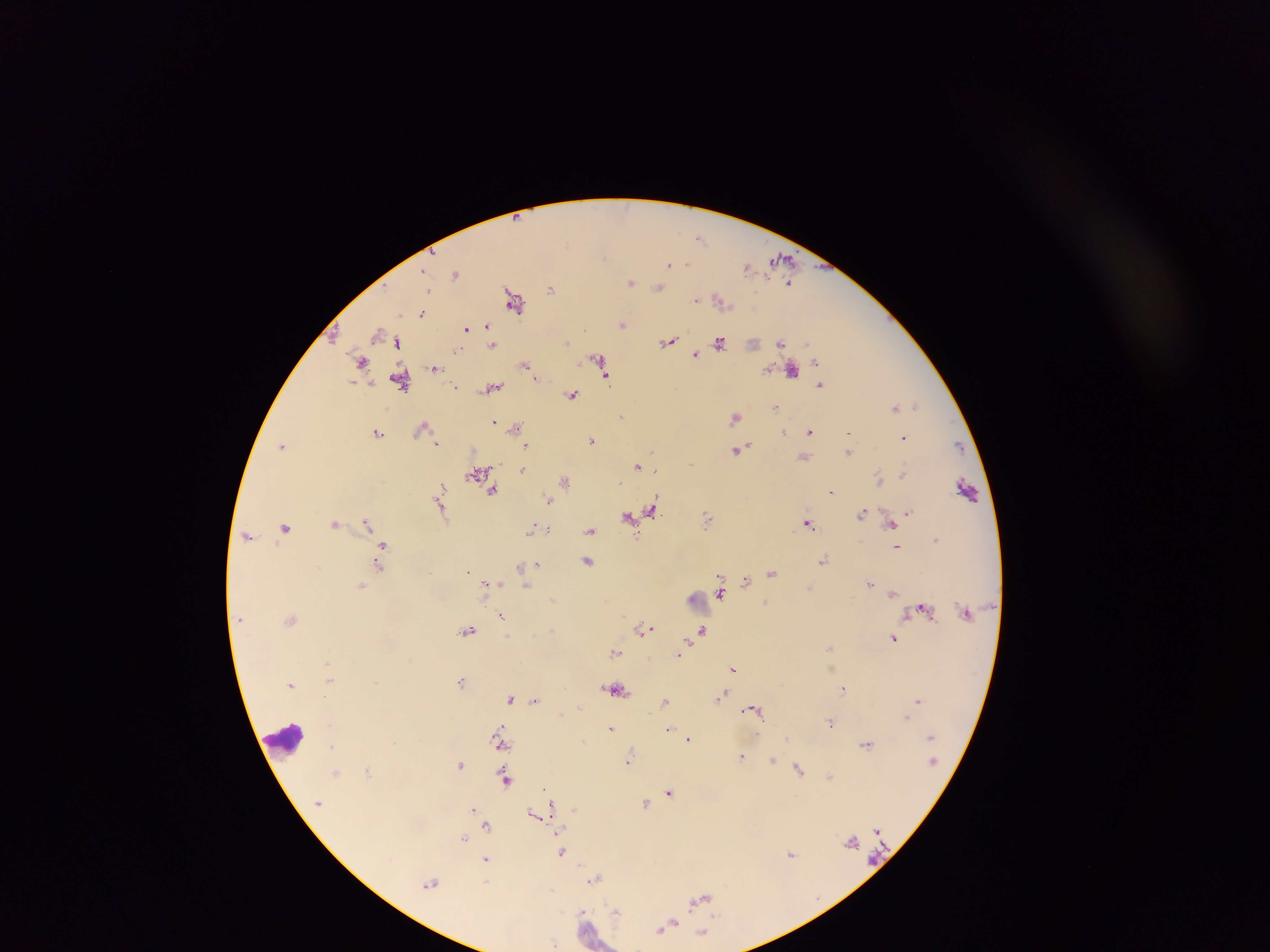

capture = mobile-phone photograph through a microscope
image size = 1270×952 pixels
field of view = single
malaria parasite locations = approximate centers as {x, y} in pixels: {700, 238}, {783, 260}, {670, 264}, {747, 266}, {425, 272}, {455, 273}, {631, 281}, {790, 283}, {659, 286}, {429, 288}, {551, 288}, {514, 299}, {696, 299}, {721, 300}, {422, 314}, {623, 323}, {488, 326}, {466, 327}, {399, 340}, {669, 341}, {719, 342}, {754, 342}, {782, 343}, {493, 344}, {695, 353}, {601, 359}, {816, 360}, {362, 361}, {526, 365}, {435, 367}, {768, 368}, {792, 369}, {607, 374}, {401, 380}, {354, 383}, {821, 383}, {455, 386}, {493, 387}, {572, 395}, {918, 405}, {895, 407}, {774, 409}, {622, 415}, {735, 416}, {496, 421}, {424, 426}, {515, 427}, {811, 430}, {849, 431}, {784, 432}, {378, 433}, {904, 437}, {592, 439}, {437, 443}, {959, 444}, {527, 445}, {283, 446}, {740, 449}, {849, 451}, {804, 457}, {692, 464}, {639, 465}, {523, 470}, {479, 472}, {903, 474}, {880, 478}, {565, 480}, {441, 486}, {968, 489}, {492, 491}, {831, 491}, {550, 500}, {441, 504}, {653, 507}, {908, 512}, {863, 513}, {630, 516}, {708, 518}, {808, 522}, {892, 522}, {335, 523}, {367, 523}, {285, 527}, {549, 529}, {534, 530}, {541, 530}, {590, 530}, {248, 535}, {383, 544}, {897, 546}, {587, 560}, {824, 560}, {537, 564}, {378, 566}, {521, 567}, {468, 570}, {772, 572}, {747, 579}, {870, 582}, {486, 584}, {526, 584}, {362, 585}, {721, 590}, {894, 591}, {719, 593}, {694, 597}, {924, 608}, {502, 615}, {291, 618}, {643, 627}, {469, 629}, {704, 630}, {894, 637}, {688, 642}, {830, 646}, {615, 651}, {678, 654}, {734, 668}, {329, 678}, {462, 680}, {376, 681}, {291, 684}, {845, 687}, {616, 688}, {724, 694}, {324, 695}, {511, 698}, {535, 700}, {917, 700}, {665, 701}, {754, 709}, {907, 718}, {831, 720}, {501, 725}, {668, 727}, {611, 728}, {688, 739}, {867, 744}, {502, 745}, {742, 756}, {773, 759}, {628, 760}, {461, 764}, {800, 767}, {368, 771}, {336, 772}, {831, 775}, {506, 778}, {546, 788}, {670, 791}, {646, 803}, {552, 805}, {473, 809}, {575, 809}, {536, 815}, {487, 825}, {877, 829}, {560, 830}, {464, 837}, {852, 842}, {562, 851}, {792, 853}, {487, 860}, {594, 879}, {431, 883}, {486, 883}, {551, 891}, {701, 897}, {585, 911}, {616, 911}, {666, 926}, {661, 930}, {704, 932}, {554, 943}
preparation = thick blood smear
country = Ghana
leukocyte locations = approximate centers as {x, y} in pixels: {287, 738}